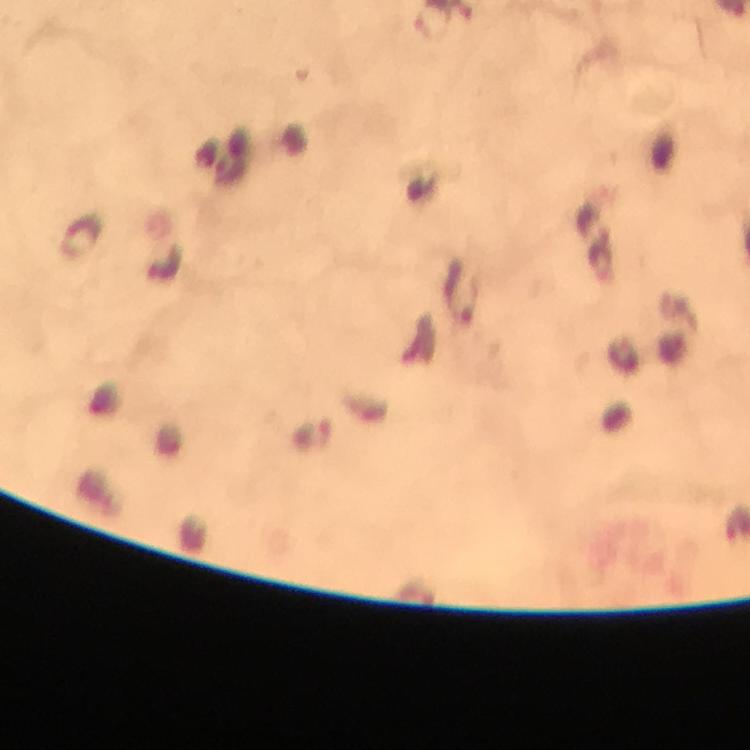
Approximate centers as {x, y} in pixels. Malaria parasite locations: {457, 293}. Cropped region of a single field of view. At 100x magnification. Giemsa stain. Smartphone photograph taken through a microscope. Thick smear. Image is 750×750 pixels. From a malaria diagnostic workup. Immersion oil was used.